Report the malaria status of this cell.
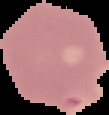

It is uninfected.

Summary:
  - Preparation: thin blood smear
  - Image type: segmented cell region with the area outside set to black
  - Image size: 109×115 pixels